State which parasite is depicted.
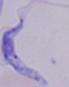

A trypanosome.

modality: photomicrograph
magnification: 1000x